Give the position of every leukocyte visible.
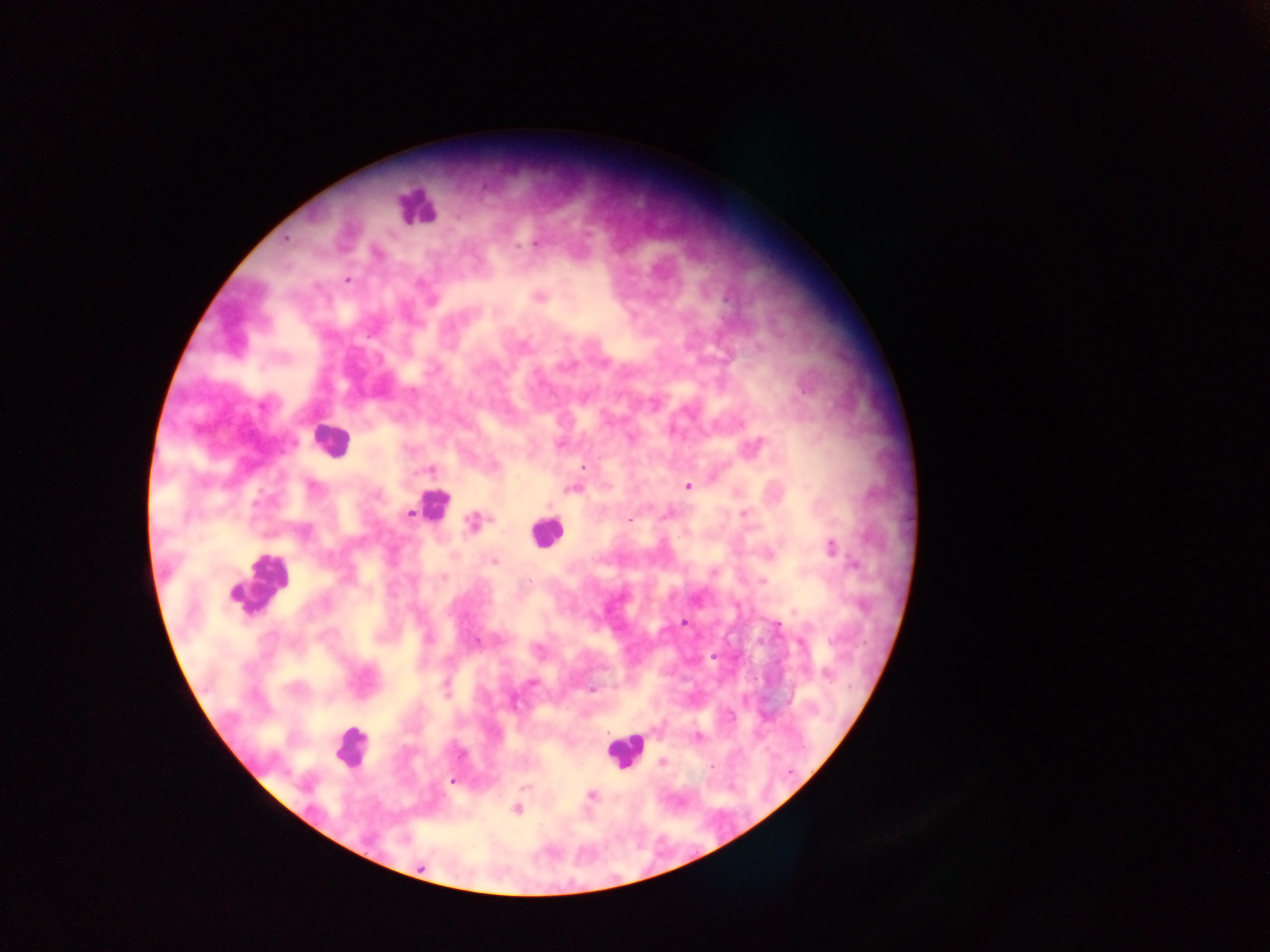
Approximate centers as x y in pixels.
Leukocytes: 416 206; 329 439; 433 504; 545 532; 262 583; 351 746; 623 751.

country = Ghana
field of view = single
malaria parasite locations = approximate centers as x y in pixels: 285 238; 536 244; 517 246; 347 279; 539 297; 432 300; 524 347; 584 397; 263 405; 630 438; 560 444; 757 445; 584 466; 431 469; 688 486; 312 487; 572 489; 377 495; 409 513; 667 514; 744 514; 629 520; 473 522; 305 532; 831 547; 494 562; 854 565; 713 572; 444 579; 530 580; 763 581; 683 622; 778 625; 429 639; 476 642; 713 656; 827 675; 532 683; 446 687; 592 690; 697 738; 461 754; 662 763; 711 766; 452 781; 526 787; 592 795; 517 809; 420 866
image size = 1270×952 pixels
capture = mobile-phone photograph through a microscope
preparation = thick blood smear